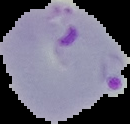
preparation = thin blood film
result = malaria parasites identified
image type = segmented cell region on a black background
image size = 130×124 pixels